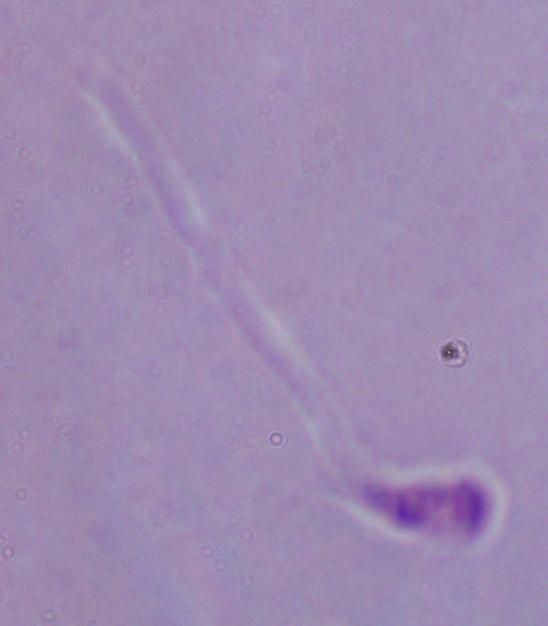

identification = Leishmania
magnification = 1000x
modality = photomicrograph